Find the cells and give the type of each one.
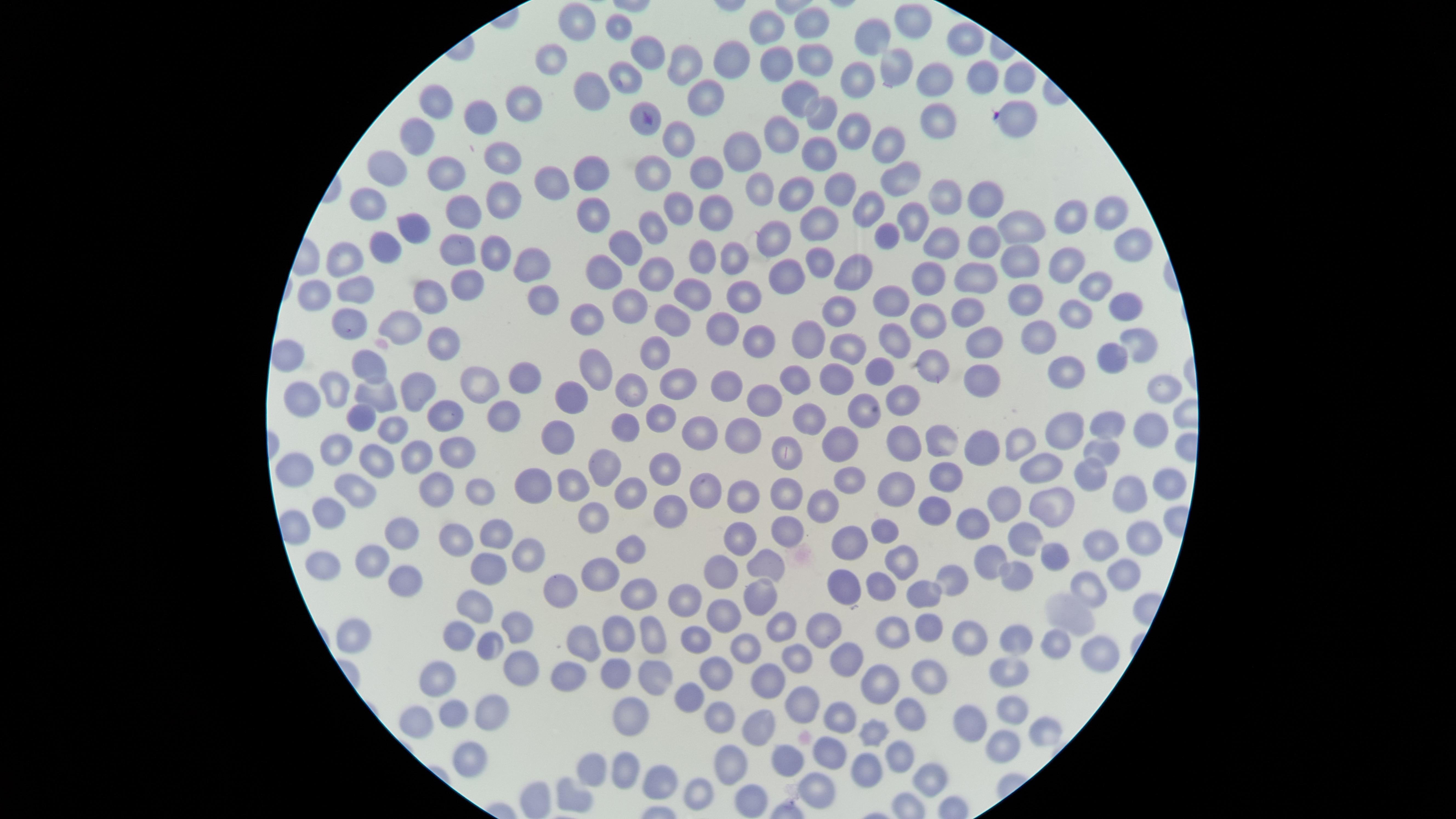

No parasitized red blood cells identified.
Approximate marker points as {x, y} in pixels.
Uninfected red blood cells: {590, 19}, {910, 21}, {814, 24}, {623, 27}, {766, 27}, {874, 35}, {966, 40}, {648, 56}, {813, 58}, {556, 60}, {729, 61}, {685, 62}, {770, 64}, {892, 71}, {983, 76}, {623, 77}, {1016, 77}, {933, 80}, {855, 81}, {797, 89}, {587, 90}, {707, 94}, {440, 100}, {526, 106}, {640, 116}, {482, 118}, {819, 118}, {936, 118}, {1022, 118}, {781, 128}, {862, 131}, {423, 132}, {680, 139}, {893, 141}, {739, 153}, {813, 153}, {499, 158}, {445, 167}, {386, 173}, {588, 173}, {654, 175}, {707, 177}, {897, 177}, {552, 181}, {758, 185}, {803, 190}, {841, 193}, {941, 194}, {498, 196}, {980, 198}, {370, 206}, {685, 208}, {716, 208}, {464, 212}, {865, 213}, {1107, 215}, {910, 216}, {1068, 216}, {590, 218}, {817, 222}, {412, 224}, {652, 224}, {1016, 224}, {778, 238}, {884, 238}, {944, 243}, {387, 244}, {977, 245}, {457, 247}, {494, 247}, {1128, 249}, {346, 251}, {631, 252}, {702, 254}, {819, 257}, {735, 258}, {1027, 260}, {1063, 261}, {854, 268}, {534, 269}, {651, 274}, {984, 274}, {608, 276}, {931, 276}, {790, 277}, {472, 284}, {1091, 284}, {313, 288}, {359, 289}, {431, 290}, {696, 296}, {743, 296}, {894, 296}, {538, 298}, {1029, 298}, {631, 307}, {1124, 307}, {962, 309}, {843, 310}, {1079, 312}, {671, 316}, {586, 319}, {933, 320}, {722, 321}, {347, 324}, {398, 327}, {1048, 335}, {898, 336}, {805, 338}, {983, 343}, {1138, 343}, {755, 344}, {850, 345}, {658, 346}, {441, 348}, {1115, 353}, {282, 356}, {931, 358}, {1071, 364}, {371, 366}, {596, 366}, {884, 368}, {975, 376}, {527, 378}, {840, 378}, {477, 382}, {794, 382}, {724, 385}, {332, 386}, {1165, 386}, {682, 387}, {630, 391}, {377, 392}, {411, 392}, {303, 398}, {571, 400}, {763, 400}, {903, 400}, {863, 405}, {808, 412}, {495, 413}, {661, 414}, {1105, 414}, {362, 415}, {449, 417}, {391, 420}, {627, 422}, {1148, 424}, {1067, 427}, {701, 432}, {746, 436}, {946, 436}, {1023, 437}, {844, 439}, {910, 439}, {561, 441}, {985, 441}, {788, 445}, {1099, 448}, {340, 452}, {458, 453}, {416, 459}, {379, 460}, {666, 464}, {607, 466}, {1048, 473}, {1089, 473}, {949, 477}, {848, 479}, {539, 481}, {1165, 481}, {435, 485}, {904, 486}, {573, 487}, {480, 490}, {705, 490}, {788, 494}, {631, 496}, {352, 497}, {1123, 497}, {1013, 499}, {1061, 500}, {747, 502}, {824, 502}, {671, 506}, {599, 507}, {320, 509}, {936, 509}, {977, 523}, {405, 531}, {788, 531}, {886, 531}, {456, 535}, {735, 535}, {497, 537}, {1024, 538}, {849, 541}, {1135, 541}, {1103, 546}, {521, 547}, {631, 548}, {1056, 553}, {377, 556}, {986, 558}, {324, 559}, {896, 562}, {766, 563}, {494, 572}, {723, 572}, {1128, 572}, {404, 574}, {946, 574}, {604, 576}, {1010, 579}, {1090, 583}, {886, 587}, {566, 588}, {847, 588}, {762, 594}, {922, 597}, {643, 601}, {477, 602}, {682, 602}, {722, 611}, {821, 622}, {779, 626}, {894, 627}, {516, 628}, {927, 628}, {612, 629}, {656, 632}, {1012, 635}, {348, 636}, {579, 636}, {965, 636}, {462, 639}, {697, 642}, {1059, 642}, {493, 644}, {1099, 647}, {748, 650}, {844, 654}, {799, 656}, {520, 662}, {1007, 665}, {568, 670}, {614, 671}, {712, 673}, {435, 674}, {656, 676}, {927, 677}, {874, 684}, {768, 685}, {686, 691}, {801, 705}, {484, 709}, {449, 710}, {905, 713}, {1011, 713}, {628, 714}, {421, 718}, {721, 719}, {840, 720}, {973, 720}, {761, 721}, {1038, 732}, {869, 737}, {1002, 742}, {828, 749}, {465, 754}, {904, 756}, {734, 761}, {790, 763}, {596, 765}, {871, 771}, {621, 773}, {658, 774}, {930, 777}, {815, 789}, {569, 795}, {694, 797}, {748, 800}.
No white blood cells identified.

Image is 1456×819 pixels. Circular visible region. Thin blood smear. Single field of view. Photographed with a smartphone camera through the microscope eyepiece. Giemsa stain.